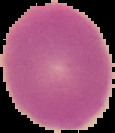

Cell region segmented out of the field of view; the surrounding area is masked to black. Image is 115×133 pixels. From a thin blood smear. Result: negative for malaria parasites.